Classify this cell by malaria status.
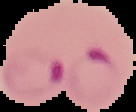
Parasitized.

image_size: 136×112 pixels
image_type: segmented cell region on a black background
preparation: thin blood smear